Locate and identify every blood parasite.
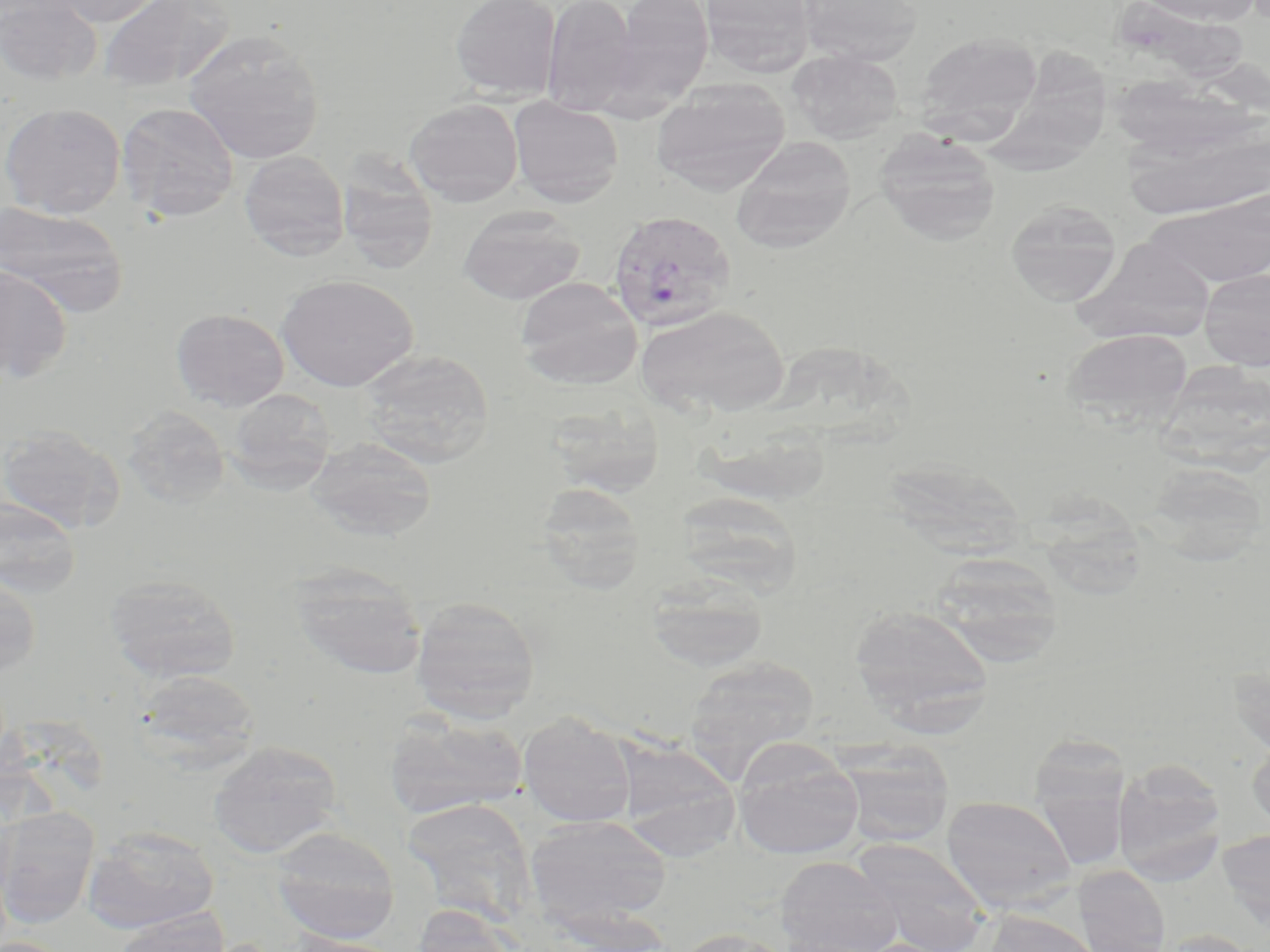

Approximate bounding boxes as (x1,y1)-(x2,y2) corner pairs in pixels.
Plasmodium vivax-infected red blood cells: (606,210)-(736,332).
No Plasmodium falciparum, Plasmodium ovale, Plasmodium malariae, Babesia divergens, or Trypanosoma brucei observed.

{
  "slide_level_diagnosis": "Plasmodium vivax",
  "magnification": "1000x",
  "image_size": "1270×952 pixels",
  "field_of_view": "one of a larger specimen",
  "stain": "May-Grünwald-Giemsa",
  "preparation": "thin blood smear",
  "modality": "light microscopy",
  "uninfected_red_blood_cell_locations": "approximate bounding boxes as (x1,y1)-(x2,y2) corner pairs in pixels: (1,0)-(101,85), (42,0)-(172,27), (98,0)-(236,94), (450,0)-(561,99), (541,0)-(640,115), (607,0)-(715,106), (700,0)-(815,77), (798,0)-(923,66), (1134,0)-(1264,26), (183,29)-(325,163), (915,31)-(1043,133), (990,35)-(1117,189), (789,49)-(903,144), (651,80)-(790,196), (508,97)-(624,207), (404,98)-(524,206), (117,102)-(240,222), (1,103)-(126,217), (1122,114)-(1270,222), (875,130)-(1001,246), (731,136)-(857,252), (239,151)-(349,260), (337,157)-(440,275), (1144,192)-(1270,287), (1005,199)-(1122,307), (0,202)-(129,318), (457,205)-(585,304), (1076,239)-(1217,343), (0,265)-(72,383), (1199,268)-(1270,370), (277,274)-(417,391), (514,276)-(643,389), (636,304)-(791,418), (171,308)-(289,411), (1064,328)-(1192,427), (358,348)-(495,469), (1162,367)-(1270,471), (225,388)-(336,493), (543,397)-(666,498), (121,406)-(231,510), (0,424)-(123,534), (304,436)-(438,541), (893,459)-(1031,556), (1142,463)-(1267,565), (534,481)-(646,593), (673,491)-(803,597), (0,496)-(83,598), (1037,499)-(1145,607), (927,552)-(1064,664), (289,563)-(428,680), (104,572)-(242,684), (0,573)-(42,677), (644,573)-(771,673), (410,595)-(541,723), (849,603)-(993,729), (682,655)-(820,780), (1228,657)-(1270,758), (130,669)-(261,772), (384,712)-(528,819), (518,712)-(636,828), (1029,734)-(1129,866), (612,736)-(741,858), (1247,738)-(1270,831), (208,740)-(342,858), (732,741)-(864,860), (834,741)-(955,847), (1113,759)-(1227,882), (941,795)-(1077,913), (402,798)-(538,924), (0,807)-(99,928), (525,815)-(672,931), (82,825)-(220,934), (270,827)-(400,943), (1217,829)-(1270,931), (850,838)-(991,952), (776,856)-(903,952), (1073,865)-(1171,952), (411,904)-(520,952), (112,910)-(229,952), (982,910)-(1103,952), (671,927)-(799,952), (1157,929)-(1258,952), (285,933)-(406,952)"
}